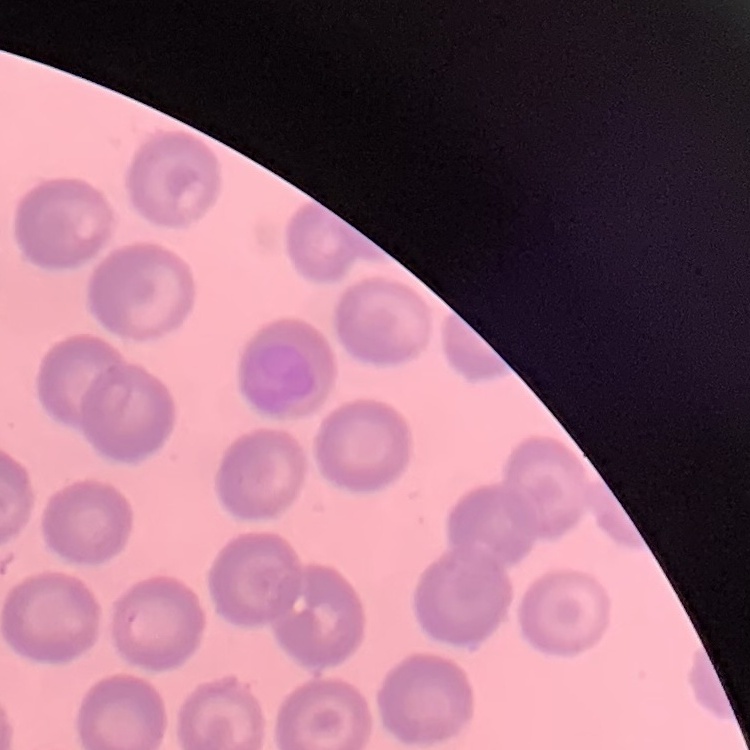

erythrocyte_morphology: no rouleaux formation
preparation: thin blood film
stain: Field's or Giemsa
image_type: one tile cut from a larger photomicrograph